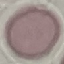

Result: negative for malaria parasites. Photographed with a smartphone camera at the microscope eyepiece. Thin smear of blood. Giemsa-stained preparation. Automatically extracted cell patch, resized to 64 × 64 pixels.